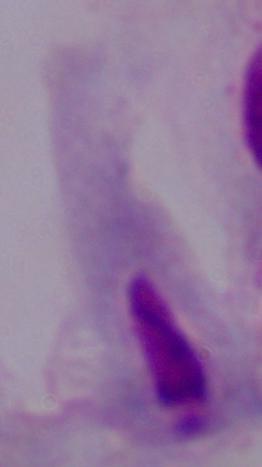

modality = micrograph
identification = trichomonad
magnification = 1000x